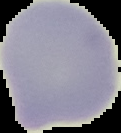
Summary:
  - Preparation: thin blood film
  - Malaria status: uninfected
  - Image size: 121×133 pixels
  - Image type: segmented cell region with the area outside set to black